Classify this cell by malaria status.
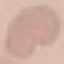

Uninfected.

capture: smartphone through the microscope eyepiece
preparation: thin smear
image_type: cell patch, automatically extracted from a larger field of view and resized to 64 × 64 pixels
stain: Giemsa